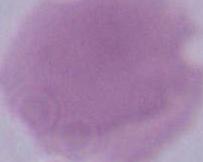

Captured at 1000x magnification. Micrograph. An erythrocyte is seen.